State which parasite is depicted.
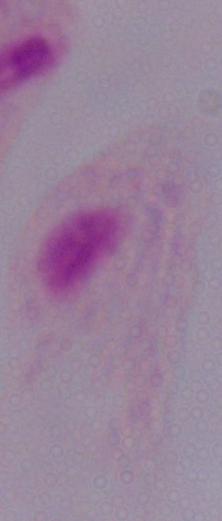
A trichomonad.

{
  "magnification": "1000x",
  "modality": "photomicrograph"
}